Give the position of every Plasmodium parasite visible.
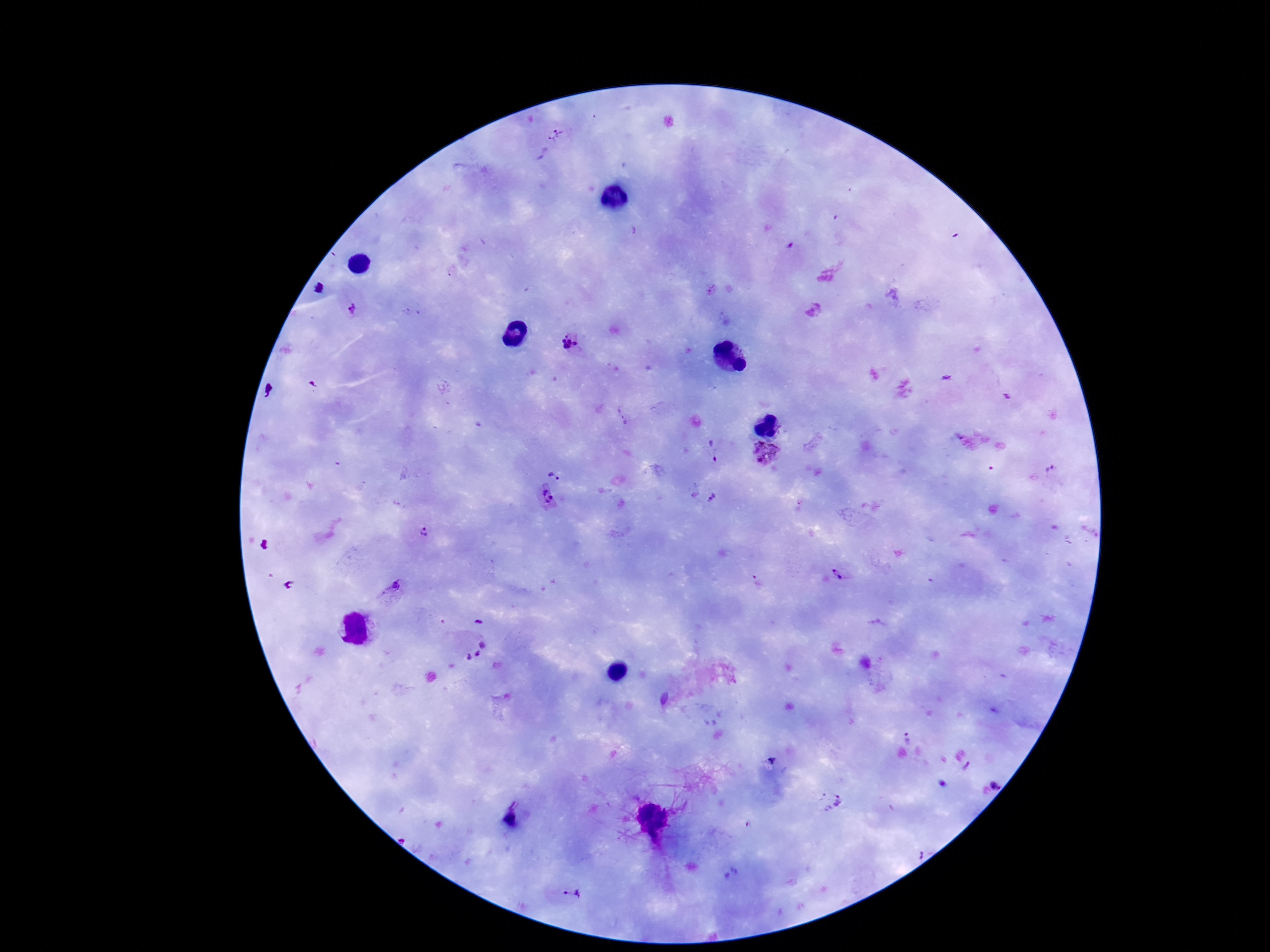

Approximate centers as [x, y] in pixels.
Plasmodium parasites: [557, 135], [318, 288], [352, 310], [569, 342], [271, 392], [622, 416], [714, 452], [766, 455], [554, 474], [693, 494], [547, 496], [713, 498], [425, 531], [264, 545], [841, 571], [759, 583], [289, 585], [391, 588], [478, 621], [474, 650], [663, 699], [907, 736], [998, 782], [829, 802], [919, 853], [571, 894].

Summary:
  - Stain: Giemsa
  - Field of view: one from this slide
  - Patient malaria status: infected
  - Magnification: 100x
  - Image size: 1270×952 pixels
  - Preparation: thick blood film
  - Capture: smartphone camera through the microscope eyepiece